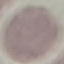
Summary:
  - Result: no malaria parasites detected
  - Preparation: thin blood film
  - Image type: cell patch, automatically extracted from a larger field of view and resized to 64 × 64 pixels
  - Capture: smartphone through the microscope eyepiece
  - Stain: Giemsa